Point out leukocytes.
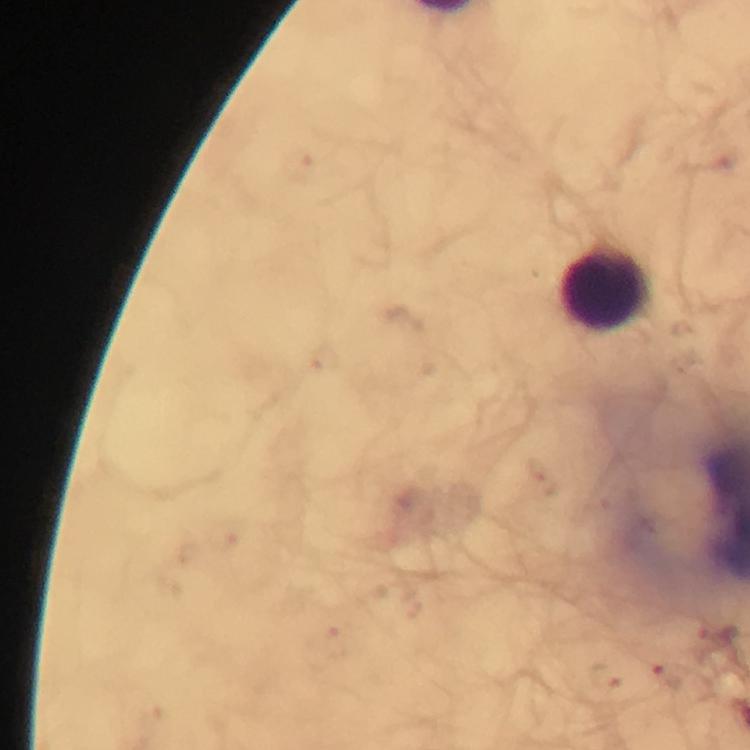

Approximate object centers, in pixels from the top-left corner.
Leukocytes: (x=604, y=285).

Smartphone photograph taken through a microscope. Thick smear. Image is 750×750 pixels. Giemsa-stained preparation. Immersion oil applied. 100x magnification. Malaria parasites: none seen. From a malaria diagnostic workup. A crop from one field of view.